Comment on the morphology of the erythrocytes.
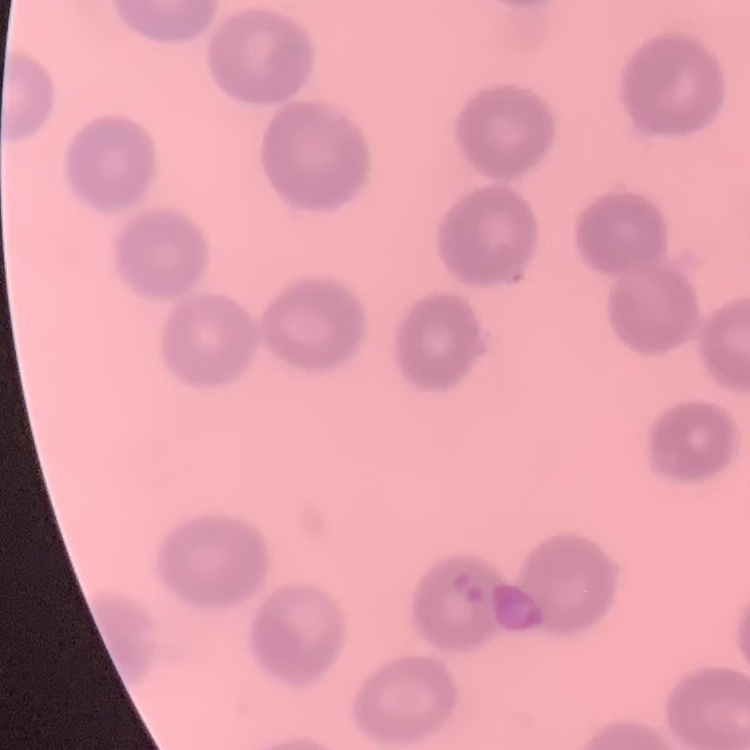
No rouleaux formation.

Square crop of a larger photomicrograph. Field's or Giemsa stain. Thin blood smear.